State which parasite is depicted.
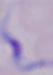

A trypanosome.

Summary:
  - Modality: micrograph
  - Magnification: 1000x